Comment on the morphology of the red blood cells.
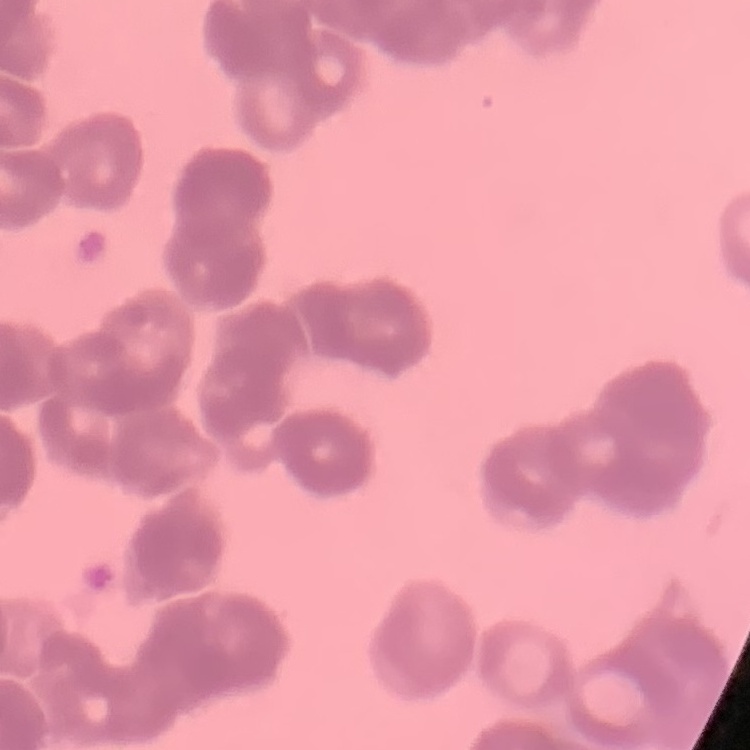

Rouleaux formation.

Summary:
  - Stain: Field's or Giemsa
  - Image type: square crop of a larger photomicrograph
  - Preparation: thin blood film